Report the malaria status of this cell.
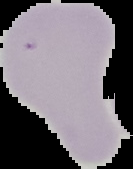
Uninfected.

image_type: cell region segmented out of the field of view; surrounding area masked to black
preparation: thin blood film
image_size: 133×169 pixels